Which red blood cells are P. falciparum-infected, and which are of indeterminate infection status?
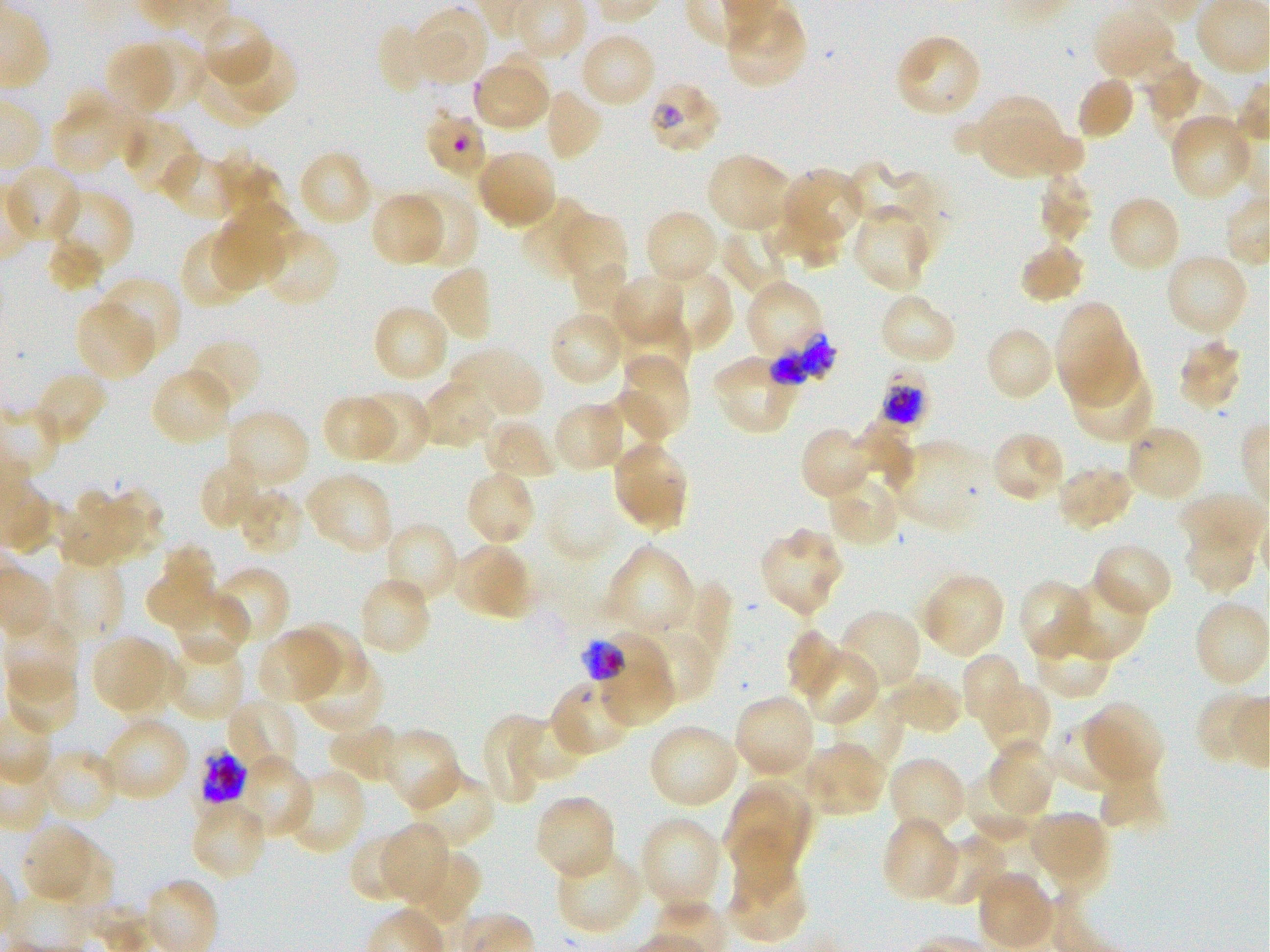

Approximate bounding boxes as [x1, y1, x2, y2] in pixels. Not every red blood cell is marked. A life-cycle stage — or a range of stages, where the recorded stages span more than one — follows each staged infected red blood cell.
Infected red blood cells: [651, 85, 721, 150] late ring to early trophozoite; [771, 333, 837, 384]; [879, 365, 929, 428] early trophozoite to early schizont; [580, 634, 673, 692] trophozoite; [198, 748, 247, 807].
Red blood cells of indeterminate infection status: [428, 113, 486, 176], [550, 676, 634, 753].

Locations of uninfected red blood cells: [412, 6, 487, 86], [1092, 7, 1176, 82], [723, 9, 806, 90], [200, 15, 273, 88], [376, 22, 436, 95], [893, 33, 983, 119], [583, 35, 653, 105], [138, 39, 207, 113], [104, 42, 174, 115], [225, 42, 297, 111], [496, 51, 549, 131], [196, 52, 276, 127], [1139, 57, 1200, 119], [473, 67, 549, 127], [1148, 71, 1229, 151], [1075, 76, 1134, 141], [542, 87, 602, 162], [978, 97, 1062, 176], [49, 101, 126, 173], [1170, 114, 1253, 200], [984, 115, 1085, 175], [120, 117, 198, 196], [161, 149, 244, 221], [298, 149, 373, 228], [475, 149, 557, 230], [705, 153, 791, 233], [217, 155, 281, 217], [845, 162, 935, 239], [5, 166, 83, 244], [784, 167, 863, 240], [1036, 173, 1094, 244], [406, 187, 479, 269], [49, 191, 134, 276], [369, 191, 444, 267], [519, 196, 595, 280], [1111, 199, 1177, 269], [225, 201, 298, 273], [851, 207, 930, 293], [774, 209, 850, 271], [644, 210, 720, 287], [559, 212, 627, 286], [212, 222, 286, 290], [719, 226, 788, 297], [179, 229, 257, 310], [258, 229, 342, 308], [47, 239, 104, 293], [1019, 241, 1086, 306], [1164, 252, 1249, 337], [573, 261, 631, 319], [429, 263, 495, 343], [659, 267, 733, 351], [611, 272, 686, 347], [99, 277, 182, 359], [745, 284, 824, 360], [878, 294, 957, 367], [74, 301, 156, 381], [372, 304, 451, 384], [1055, 306, 1124, 383], [547, 309, 626, 388], [620, 313, 693, 382], [983, 326, 1056, 403], [1060, 331, 1140, 406], [188, 337, 263, 412], [1177, 339, 1244, 412], [452, 345, 544, 420], [619, 355, 691, 440], [712, 357, 799, 430], [1070, 362, 1156, 443], [150, 368, 235, 447], [32, 372, 108, 447], [419, 378, 498, 450], [617, 389, 673, 446], [357, 391, 431, 466], [321, 394, 396, 464], [551, 402, 627, 474], [225, 409, 311, 491], [485, 417, 560, 481], [853, 418, 916, 487], [1124, 423, 1204, 502], [799, 426, 873, 502], [991, 431, 1066, 504], [612, 438, 689, 528], [891, 440, 986, 534], [197, 456, 266, 531], [1054, 465, 1135, 533], [464, 468, 537, 547], [305, 471, 393, 555], [825, 475, 901, 548], [91, 487, 164, 561], [237, 488, 307, 557], [58, 492, 133, 570], [1177, 493, 1265, 559], [383, 521, 460, 607], [758, 527, 844, 616], [1183, 528, 1257, 594], [159, 541, 216, 600], [451, 543, 533, 619], [1092, 543, 1173, 619], [603, 545, 694, 635], [49, 556, 124, 641], [145, 564, 216, 631], [212, 566, 290, 648], [920, 573, 1005, 658], [358, 575, 432, 657], [1055, 575, 1148, 663], [669, 578, 732, 666], [1018, 578, 1091, 659], [173, 590, 250, 667], [1193, 600, 1269, 689], [837, 609, 924, 693], [1035, 617, 1112, 702], [4, 620, 79, 696], [283, 620, 367, 694], [786, 628, 848, 701], [256, 629, 338, 706], [636, 634, 709, 702], [93, 638, 163, 708], [163, 639, 246, 722], [121, 643, 184, 720], [803, 645, 880, 727], [297, 652, 383, 733], [960, 653, 1025, 729], [6, 662, 79, 735], [601, 672, 673, 724], [885, 673, 964, 735], [980, 681, 1051, 757], [1194, 692, 1262, 768], [733, 693, 817, 779], [828, 694, 903, 780], [225, 698, 301, 778], [1079, 702, 1163, 787], [481, 713, 544, 806], [508, 714, 583, 785], [1048, 718, 1129, 793], [104, 720, 188, 802], [331, 721, 402, 780], [648, 724, 741, 809], [383, 728, 462, 811], [988, 739, 1056, 815], [803, 742, 884, 815], [40, 748, 119, 825], [230, 756, 315, 841], [887, 756, 967, 836], [283, 766, 366, 855], [406, 769, 495, 853], [964, 769, 1042, 843], [1099, 775, 1167, 832], [723, 778, 812, 859], [533, 793, 616, 881], [193, 807, 264, 879], [1027, 810, 1103, 879], [639, 816, 725, 913], [880, 818, 960, 902], [973, 819, 1043, 896], [379, 823, 449, 904], [1047, 823, 1107, 893], [21, 825, 106, 907], [351, 831, 423, 905], [925, 836, 1006, 906], [404, 847, 481, 927], [555, 847, 645, 937], [727, 860, 809, 944], [977, 871, 1055, 949]. P. falciparum strain 3D7 maintained in static in-vitro culture. Blood group of the donor: O+. Giemsa stain. Thin blood smear. Image is 1270×952 pixels. One field from this slide. 100x objective under oil immersion, numerical aperture 1.25.